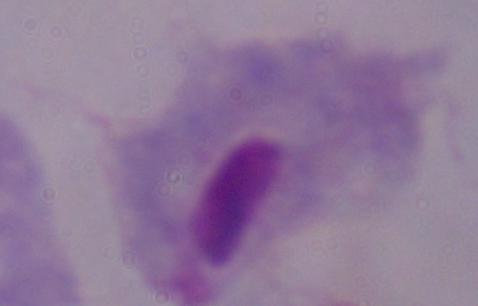
Summary:
  - Identification: trichomonad
  - Magnification: 1000x
  - Modality: photomicrograph